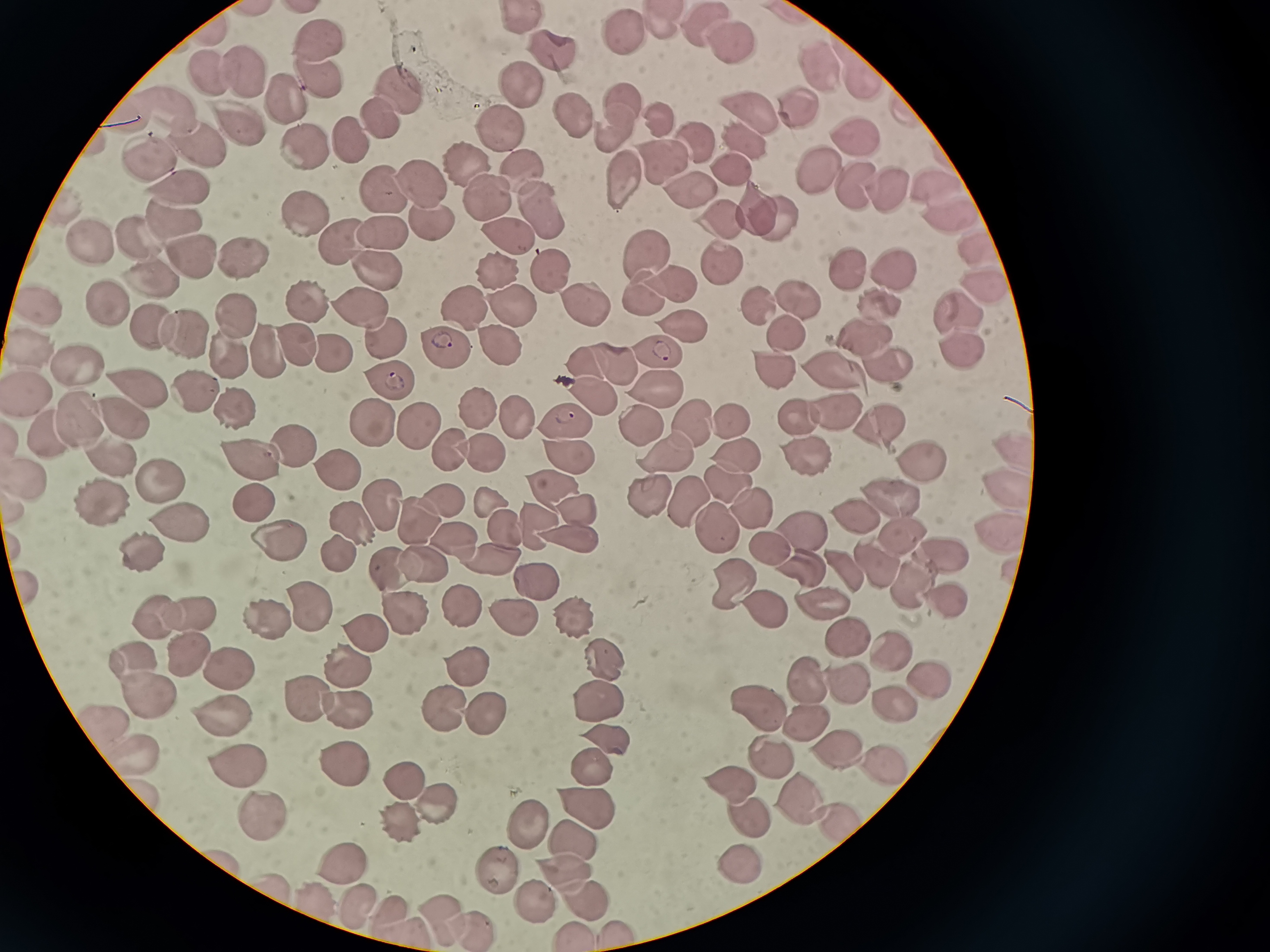

Approximate object centers, in pixels from the top-left corner. Cell locations: (x=523, y=19), (x=660, y=21), (x=707, y=26), (x=624, y=34), (x=320, y=42), (x=732, y=43), (x=547, y=49), (x=817, y=71), (x=323, y=73), (x=242, y=74), (x=856, y=76), (x=208, y=79), (x=520, y=84), (x=399, y=89), (x=283, y=96), (x=618, y=103), (x=792, y=109), (x=573, y=113), (x=748, y=113), (x=374, y=114), (x=168, y=115), (x=659, y=118), (x=237, y=126), (x=498, y=128), (x=612, y=128), (x=348, y=136), (x=197, y=138), (x=854, y=138), (x=690, y=139), (x=302, y=141), (x=747, y=143), (x=661, y=158), (x=467, y=164), (x=152, y=166), (x=731, y=166), (x=821, y=169), (x=522, y=176), (x=618, y=178), (x=861, y=182), (x=424, y=184), (x=385, y=188), (x=889, y=188), (x=183, y=190), (x=937, y=191), (x=690, y=193), (x=488, y=199), (x=755, y=203), (x=539, y=212), (x=308, y=213), (x=772, y=216), (x=430, y=222), (x=949, y=222), (x=720, y=224), (x=174, y=225), (x=386, y=228), (x=138, y=240), (x=91, y=241), (x=509, y=243), (x=343, y=246), (x=974, y=247), (x=655, y=254), (x=245, y=255), (x=190, y=256), (x=719, y=262), (x=376, y=266), (x=891, y=266), (x=493, y=270), (x=845, y=270), (x=542, y=272), (x=148, y=275), (x=672, y=282), (x=980, y=289), (x=649, y=291), (x=794, y=293), (x=883, y=302), (x=106, y=303), (x=582, y=303), (x=306, y=305), (x=759, y=305), (x=42, y=306), (x=508, y=306), (x=959, y=307), (x=466, y=308), (x=361, y=309), (x=230, y=315), (x=151, y=325), (x=680, y=325), (x=787, y=331), (x=189, y=332), (x=382, y=336), (x=871, y=336), (x=494, y=337), (x=293, y=341), (x=34, y=343), (x=441, y=346), (x=272, y=348), (x=657, y=348), (x=229, y=351), (x=960, y=351), (x=326, y=352), (x=611, y=362), (x=583, y=363), (x=888, y=364), (x=81, y=367), (x=769, y=369), (x=829, y=371), (x=386, y=378), (x=141, y=381), (x=655, y=382), (x=194, y=383), (x=33, y=394), (x=592, y=395), (x=226, y=404), (x=118, y=409), (x=477, y=409), (x=837, y=410), (x=796, y=412), (x=76, y=414), (x=515, y=418), (x=643, y=418), (x=367, y=419), (x=571, y=421), (x=691, y=421), (x=730, y=421), (x=881, y=422), (x=418, y=425), (x=53, y=439), (x=289, y=442), (x=450, y=446), (x=669, y=449), (x=1018, y=449), (x=564, y=450), (x=479, y=451), (x=807, y=451), (x=105, y=456), (x=736, y=456), (x=248, y=461), (x=921, y=461), (x=335, y=464), (x=29, y=474), (x=153, y=481), (x=727, y=481), (x=1005, y=483), (x=550, y=484), (x=651, y=490), (x=100, y=492), (x=685, y=494), (x=889, y=498), (x=253, y=502), (x=494, y=502), (x=443, y=503), (x=748, y=504), (x=383, y=506), (x=579, y=507), (x=852, y=515), (x=177, y=517), (x=348, y=518), (x=420, y=521), (x=537, y=522), (x=503, y=524), (x=713, y=524), (x=800, y=526), (x=996, y=529), (x=899, y=531), (x=453, y=534), (x=571, y=537), (x=277, y=545), (x=769, y=545), (x=142, y=549), (x=337, y=552), (x=936, y=552), (x=486, y=554), (x=421, y=561), (x=877, y=564), (x=805, y=565), (x=845, y=567), (x=391, y=571), (x=535, y=576), (x=737, y=578), (x=908, y=584), (x=310, y=597), (x=946, y=598), (x=399, y=601), (x=761, y=603), (x=820, y=603), (x=457, y=604), (x=185, y=607), (x=262, y=607), (x=510, y=607), (x=158, y=609), (x=576, y=613). Giemsa stain. Image is 1270×952 pixels. Single field of view. Acquired by smartphone through the microscope eyepiece. Thin smear of blood.